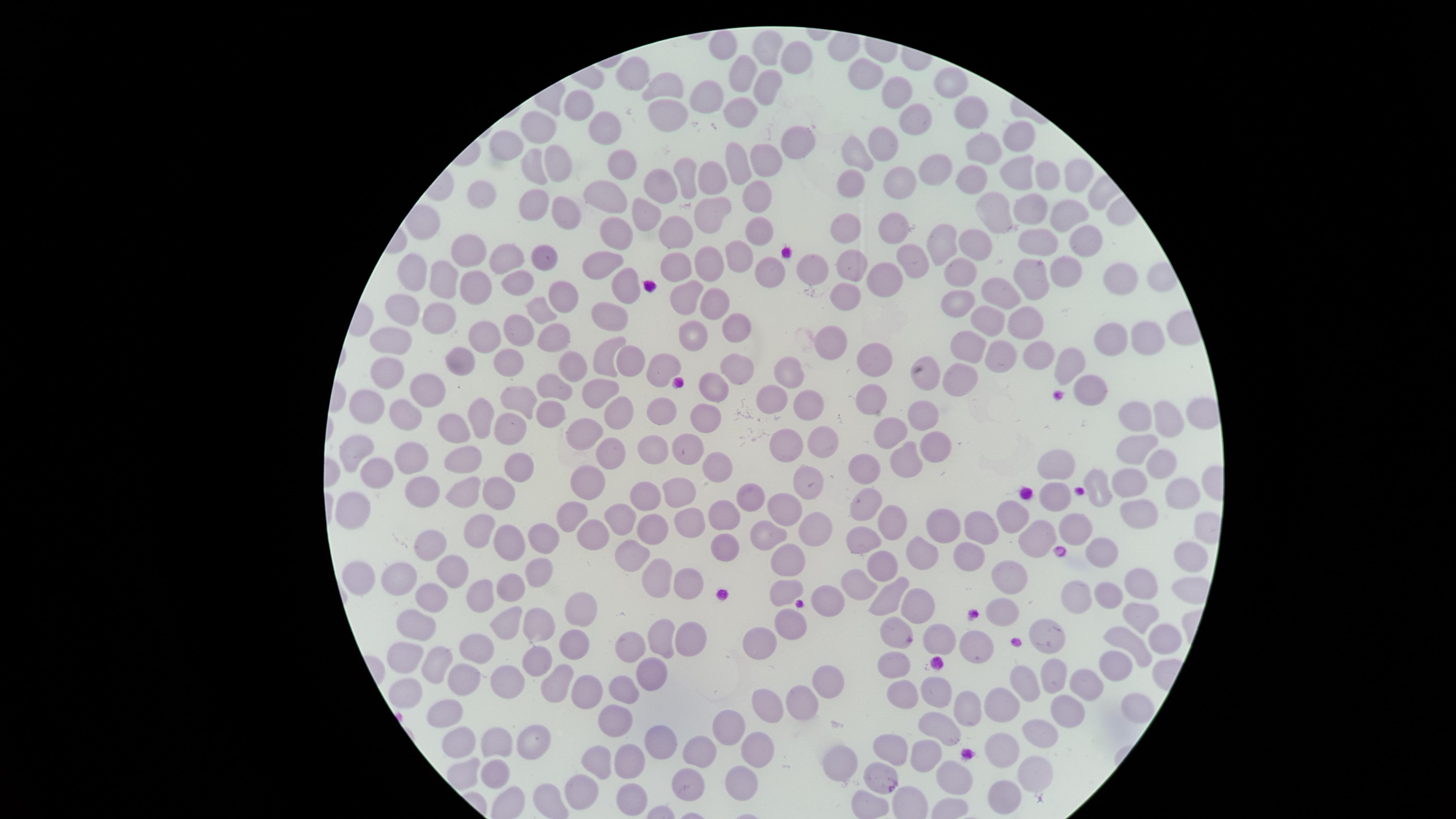

{
  "uninfected_red_blood_cells": "approximate marker points as [x, y] in pixels: [723, 46], [769, 49], [796, 62], [631, 71], [862, 72], [741, 75], [946, 82], [762, 87], [668, 88], [897, 94], [712, 98], [734, 111], [579, 114], [667, 114], [971, 116], [913, 119], [539, 125], [614, 133], [1019, 135], [796, 141], [885, 148], [507, 150], [985, 150], [855, 154], [769, 162], [738, 163], [562, 164], [528, 168], [624, 169], [935, 172], [1072, 172], [716, 173], [1022, 173], [684, 174], [977, 176], [1047, 176], [656, 182], [853, 182], [892, 188], [755, 196], [480, 200], [596, 202], [559, 205], [528, 206], [711, 212], [1032, 212], [999, 216], [640, 217], [1064, 218], [849, 225], [757, 231], [892, 231], [616, 232], [674, 234], [978, 240], [1038, 240], [1087, 240], [943, 244], [466, 252], [506, 258], [543, 258], [712, 260], [910, 260], [737, 262], [602, 265], [676, 265], [811, 266], [849, 267], [957, 269], [770, 271], [1064, 273], [884, 277], [1031, 277], [415, 278], [1124, 281], [517, 282], [623, 282], [445, 283], [470, 287], [1000, 292], [559, 294], [842, 297], [688, 299], [712, 304], [955, 307], [407, 311], [536, 312], [442, 316], [612, 316], [739, 321], [992, 321], [1025, 323], [517, 327], [481, 336], [553, 337], [694, 338], [1107, 338], [1137, 340], [832, 342], [395, 345], [967, 345], [1040, 355], [611, 356], [1000, 357], [878, 360], [461, 361], [509, 361], [627, 361], [567, 362], [1063, 366], [660, 368], [738, 368], [790, 370], [392, 372], [927, 378], [957, 378], [713, 386], [558, 388], [430, 389], [601, 391], [1094, 394], [529, 396], [868, 398], [377, 400], [774, 402], [812, 405], [555, 411], [660, 412], [406, 414], [618, 414], [477, 417], [710, 417], [925, 419], [1130, 419], [1171, 422], [452, 425], [510, 426], [888, 430], [587, 434], [826, 441], [652, 442], [789, 442], [686, 447], [939, 447], [1137, 453], [361, 454], [413, 454], [611, 455], [906, 458], [467, 462], [718, 465], [1059, 466], [521, 467], [865, 469], [1159, 469], [380, 473], [587, 476], [1092, 479], [809, 482], [1130, 483], [418, 488], [680, 491], [1171, 491], [752, 492], [642, 493], [469, 494], [505, 494], [1060, 499], [862, 503], [782, 507], [362, 511], [569, 512], [1141, 513], [1013, 514], [685, 517], [620, 519], [892, 519], [719, 522], [651, 527], [816, 527], [940, 527], [983, 527], [484, 530], [598, 531], [1080, 531], [766, 534], [548, 539], [724, 541], [870, 541], [1030, 541], [436, 543], [507, 544], [631, 553], [919, 553], [1107, 553], [1185, 553], [966, 554], [792, 560], [887, 567], [456, 570], [537, 572], [362, 577], [402, 577], [658, 577], [1002, 578], [685, 580], [864, 580], [1138, 580], [785, 587], [482, 592], [511, 592], [1078, 592], [888, 595], [439, 597], [835, 599], [1099, 600], [1005, 602], [579, 604], [915, 604], [1133, 614], [790, 620], [540, 622], [506, 623], [416, 628], [895, 630], [1055, 636], [685, 637], [1150, 637], [943, 638], [664, 639], [578, 640], [973, 640], [763, 642], [1125, 645], [636, 648], [478, 649], [405, 655], [443, 660], [539, 664], [895, 664], [1110, 667], [651, 672], [1055, 672], [1026, 679], [462, 685], [511, 685], [557, 685], [832, 685], [1084, 686], [621, 688], [406, 693], [591, 693], [903, 693], [931, 693], [798, 697], [765, 705], [961, 705], [1004, 707], [1062, 714], [612, 718], [439, 720], [729, 725], [939, 733], [1037, 737], [656, 739], [456, 740], [535, 740], [507, 745], [890, 745], [753, 747], [1004, 747], [705, 750], [931, 755], [844, 758], [625, 760], [600, 761], [1032, 773], [876, 774], [488, 776], [962, 779], [739, 780], [591, 786], [685, 787], [631, 794], [1004, 795]",
  "stain": "Giemsa",
  "preparation": "thin smear of blood",
  "presence": "no malaria parasites identified",
  "field_of_view": "single",
  "capture": "smartphone photograph through the microscope eyepiece",
  "visible_region": "circular",
  "image_size": "1456×819 pixels"
}